Assess the morphology of the erythrocytes.
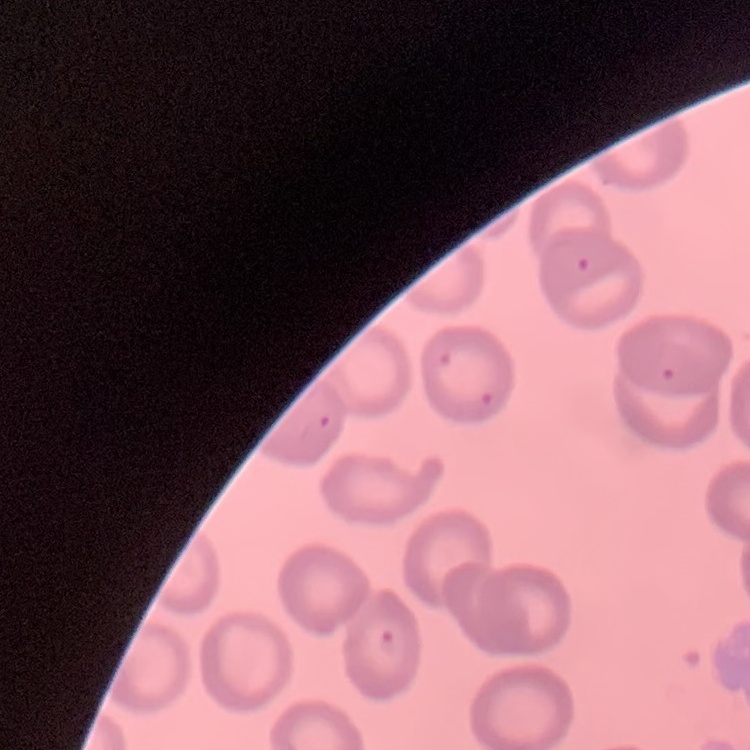
No rouleaux formation.

Summary:
  - Stain: Field's or Giemsa
  - Image type: one tile cut from a larger photomicrograph
  - Preparation: thin peripheral smear